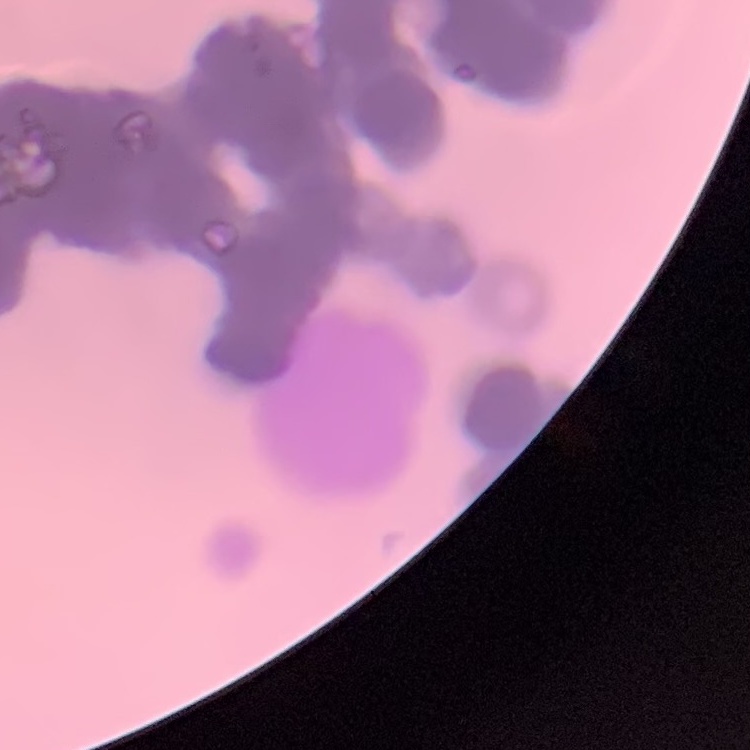

Summary:
  - Erythrocyte morphology: rouleaux formation
  - Image type: square crop of a larger photomicrograph
  - Stain: Field's or Giemsa
  - Preparation: thin blood film